Locate and identify every blood parasite.
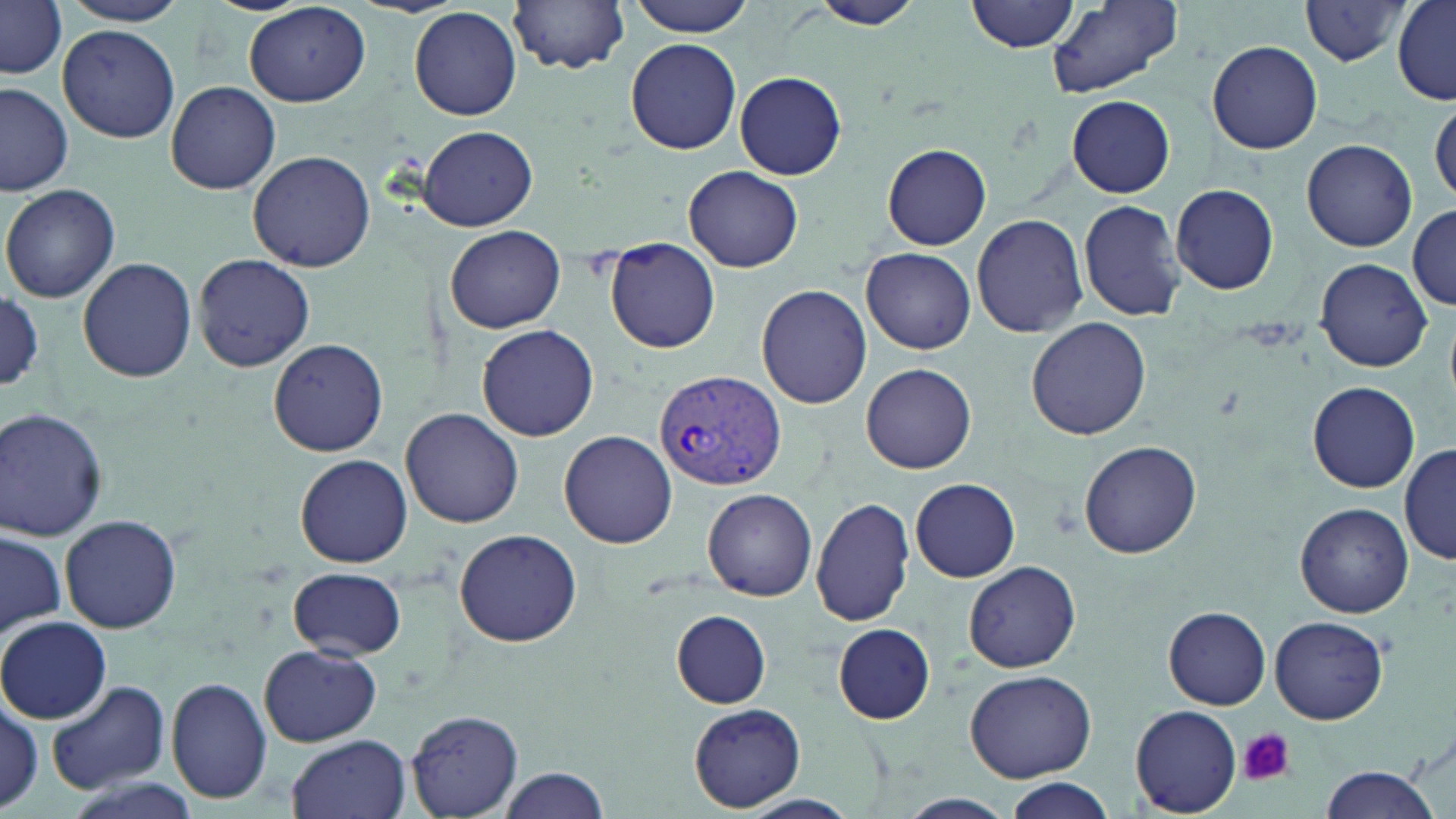
Approximate bounding boxes as (x1,y1)-(x2,y2) corner pairs in pixels.
Plasmodium vivax-infected red blood cells: (654,367)-(787,495).
No Plasmodium falciparum, Plasmodium ovale, Plasmodium malariae, Babesia divergens, or Trypanosoma brucei observed.

Platelet locations: (1237,727)-(1293,786). Uninfected red blood cell locations: (59,0)-(190,28), (621,0)-(761,35), (968,0)-(1085,53), (1391,0)-(1455,104), (510,1)-(631,73), (803,1)-(925,32), (1298,1)-(1415,66), (2,2)-(68,78), (1047,2)-(1182,99), (243,4)-(372,107), (409,6)-(522,120), (57,23)-(181,143), (626,37)-(742,155), (1207,39)-(1324,155), (734,71)-(847,179), (165,81)-(281,195), (0,83)-(74,196), (1066,94)-(1174,198), (1429,95)-(1455,207), (419,125)-(537,231), (1301,139)-(1417,252), (883,144)-(991,249), (247,149)-(375,273), (683,165)-(803,272), (1,181)-(120,303), (1171,183)-(1280,295), (1078,199)-(1186,321), (1409,204)-(1456,309), (970,212)-(1089,337), (444,225)-(567,333), (605,239)-(721,354), (862,248)-(976,353), (192,253)-(314,373), (78,257)-(197,383), (1315,258)-(1432,370), (755,283)-(872,409), (0,291)-(44,390), (1025,318)-(1152,441), (476,323)-(599,442), (268,337)-(388,458), (861,363)-(976,473), (1306,381)-(1422,493), (0,407)-(109,540), (401,408)-(526,530), (558,430)-(678,548), (1079,439)-(1202,559), (1399,445)-(1454,566), (295,453)-(413,568), (910,478)-(1020,582), (703,488)-(818,601), (810,496)-(916,627), (1294,502)-(1414,619), (59,513)-(182,634), (1,529)-(66,642), (453,529)-(583,647), (964,561)-(1081,673), (288,566)-(406,658), (1163,607)-(1272,709), (671,610)-(773,707), (1,615)-(111,722), (1270,616)-(1388,725), (832,622)-(937,724), (12,623)-(155,779), (260,644)-(382,747), (965,669)-(1096,782), (164,677)-(271,808), (45,678)-(171,796), (0,697)-(43,814), (686,704)-(808,811), (1131,705)-(1243,814), (407,708)-(524,817), (287,734)-(410,819), (1316,764)-(1442,819), (498,767)-(611,819), (999,777)-(1119,819), (901,792)-(1014,817), (737,794)-(860,819). Slide-level diagnosis: Plasmodium vivax. Single field of view. May-Grünwald-Giemsa-stained preparation. Thin blood film. Image is 1456×819 pixels. Light microscopy. 1000x magnification.